Identify the cell.
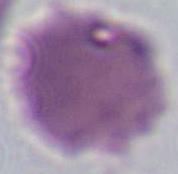
This is an erythrocyte.

Micrograph. 1000x magnification.